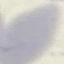

Summary:
  - Malaria status: uninfected
  - Preparation: thin blood film
  - Image type: cell patch, automatically extracted from a larger field of view and resized to 64 × 64 pixels
  - Capture: smartphone through the microscope eyepiece
  - Stain: Giemsa